State which parasite is depicted.
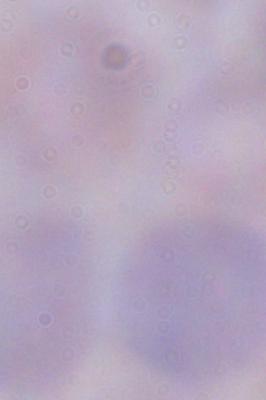

This is a trypanosome.

Summary:
  - Modality: micrograph
  - Magnification: 1000x